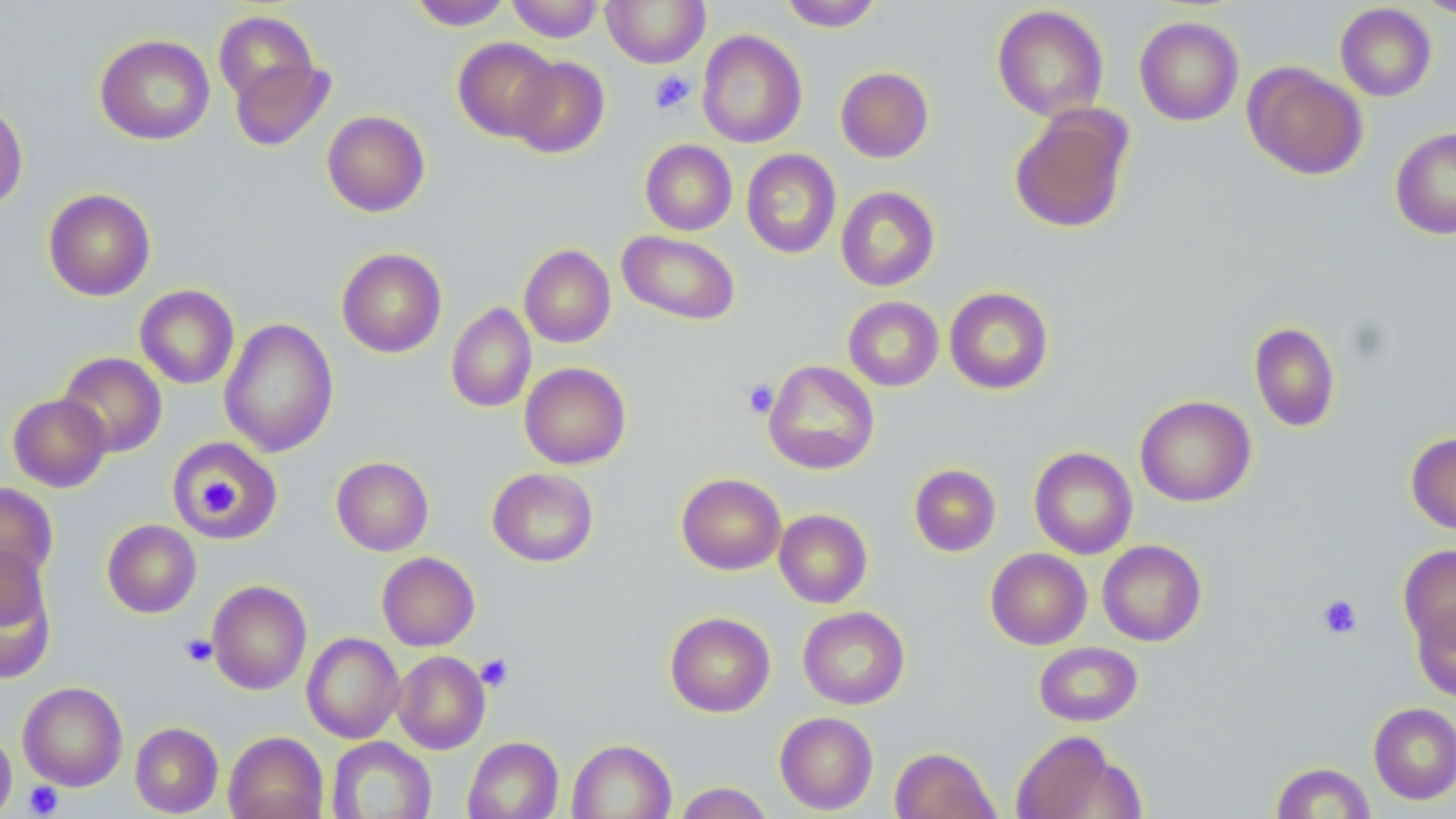

Summary:
  - Coordinate format: approximate bounding boxes as [x1, y1, x2, y2] in pixels
  - Uninfected red blood cell locations: [507, 0, 604, 42], [602, 0, 710, 68], [780, 0, 883, 31], [1415, 0, 1455, 20], [408, 1, 513, 30], [1335, 3, 1437, 102], [991, 4, 1109, 121], [213, 10, 320, 108], [1134, 16, 1244, 126], [697, 30, 807, 149], [95, 34, 215, 145], [453, 37, 559, 142], [229, 56, 334, 152], [508, 56, 610, 158], [1243, 62, 1368, 181], [835, 66, 934, 163], [0, 98, 28, 213], [1009, 107, 1133, 235], [321, 110, 430, 217], [1390, 127, 1456, 239], [640, 140, 737, 235], [742, 148, 841, 259], [836, 186, 940, 291], [43, 188, 156, 301], [617, 230, 741, 326], [519, 244, 616, 348], [336, 247, 447, 358], [135, 284, 239, 389], [944, 287, 1054, 395], [843, 296, 944, 391], [446, 303, 536, 413], [219, 317, 339, 458], [1249, 322, 1340, 433], [58, 352, 167, 457], [763, 360, 880, 474], [519, 362, 631, 469], [8, 393, 112, 492], [1134, 395, 1256, 507], [1406, 432, 1456, 535], [167, 436, 283, 543], [1029, 447, 1138, 559], [331, 456, 434, 556], [909, 463, 1001, 557], [487, 467, 599, 567], [677, 473, 787, 575], [0, 482, 58, 588], [774, 509, 872, 608], [102, 519, 202, 618], [1097, 540, 1207, 646], [1398, 544, 1456, 649], [985, 548, 1092, 650], [377, 552, 480, 651], [0, 557, 56, 685], [207, 579, 312, 695], [1411, 601, 1456, 701], [798, 606, 910, 709], [665, 611, 776, 717], [301, 632, 404, 744], [1034, 641, 1143, 727], [393, 650, 490, 754], [17, 681, 128, 789], [1369, 702, 1456, 805], [774, 711, 878, 814], [130, 722, 223, 816], [0, 727, 17, 819], [1009, 730, 1140, 819], [223, 731, 328, 819], [326, 736, 437, 819], [463, 736, 564, 819], [568, 739, 676, 819], [890, 747, 1000, 819], [1269, 761, 1376, 819], [673, 781, 775, 819]
  - Platelet locations: [649, 70, 696, 114], [742, 379, 778, 418], [192, 475, 238, 519], [1317, 594, 1363, 640], [181, 634, 217, 667], [475, 653, 514, 692], [23, 781, 63, 817]
  - Slide-level diagnosis: no evidence of blood parasites
  - Stain: May-Grünwald-Giemsa
  - Preparation: thin blood film
  - Image size: 1456×819 pixels
  - Field of view: one of a larger specimen
  - Magnification: 1000x
  - Modality: light microscopy